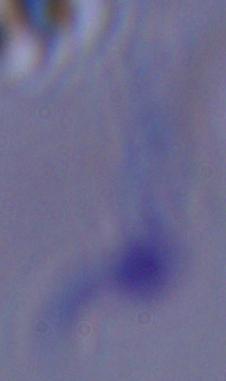
Summary:
  - Modality: photomicrograph
  - Identification: trypanosome
  - Magnification: 1000x